Name the parasite shown.
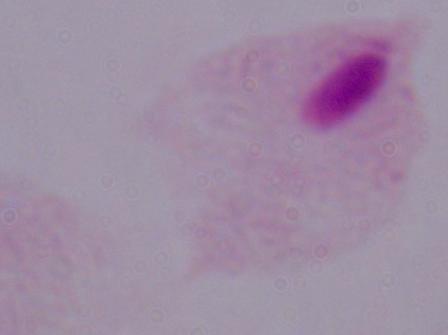
A trichomonad.

Summary:
  - Modality: micrograph
  - Magnification: 1000x